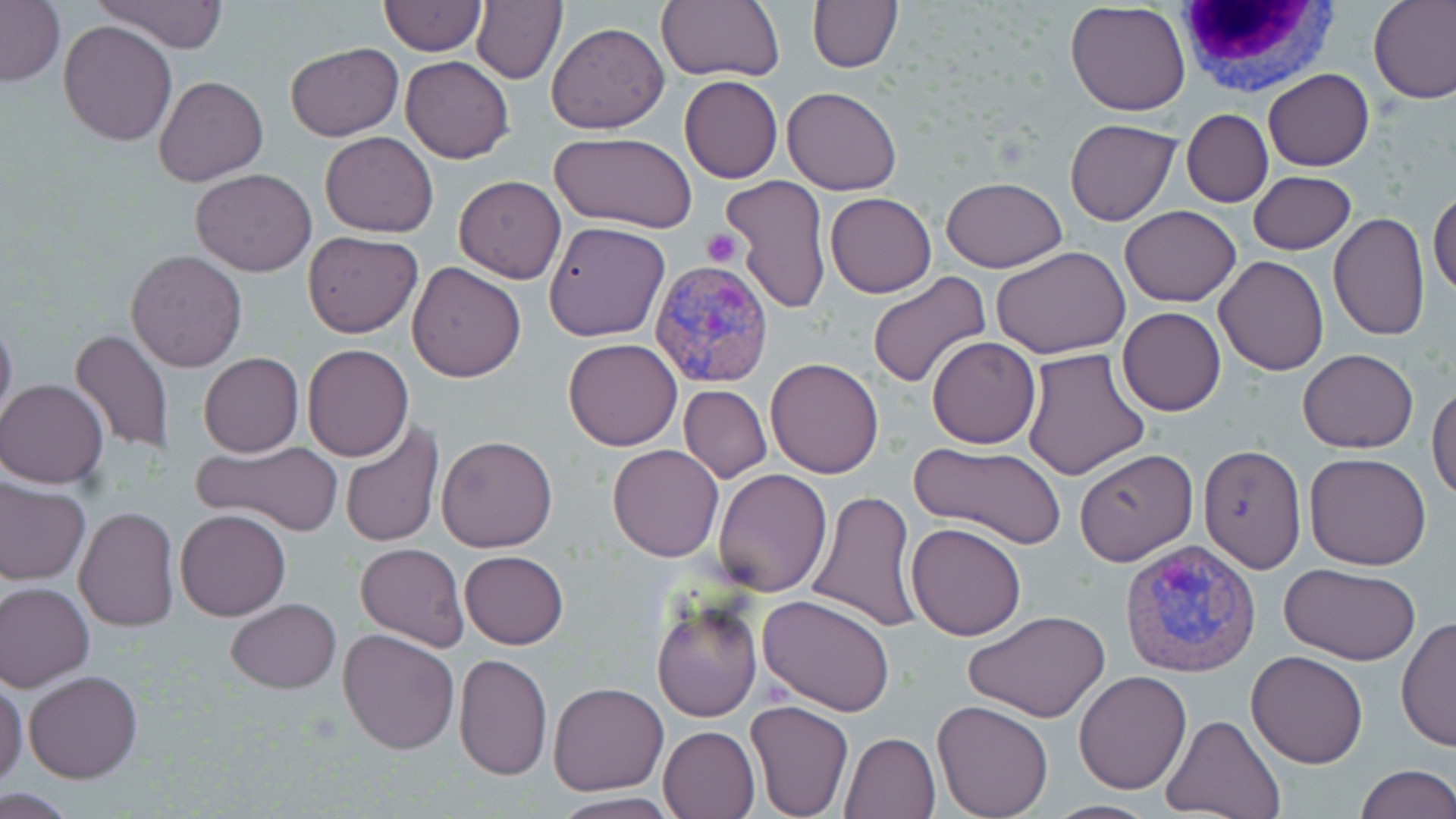
Approximate bounding boxes as (x1, y1, x2, y2) in pixels. White blood cell locations: (1173, 0, 1340, 103). Platelet locations: (702, 228, 744, 268). Uninfected red blood cell locations: (93, 0, 229, 53), (471, 0, 567, 85), (657, 0, 785, 81), (807, 0, 901, 73), (1369, 0, 1456, 105), (380, 1, 486, 55), (1, 2, 64, 87), (1065, 3, 1192, 116), (58, 21, 178, 147), (546, 21, 669, 133), (285, 42, 404, 141), (401, 57, 515, 164), (1263, 68, 1374, 171), (154, 75, 268, 187), (680, 76, 783, 183), (782, 86, 902, 196), (1183, 110, 1272, 207), (1065, 119, 1180, 226), (319, 131, 438, 237), (551, 133, 698, 235), (190, 169, 316, 276), (1250, 171, 1356, 255), (722, 174, 832, 313), (1266, 174, 1397, 286), (454, 175, 567, 284), (941, 176, 1066, 272), (1429, 187, 1456, 298), (824, 192, 935, 298), (1120, 205, 1240, 306), (1328, 213, 1430, 341), (542, 221, 669, 342), (303, 233, 421, 337), (991, 244, 1130, 359), (126, 249, 248, 372), (1213, 255, 1328, 376), (408, 262, 527, 382), (867, 273, 991, 390), (0, 305, 17, 436), (1117, 307, 1226, 416), (67, 328, 175, 457), (927, 337, 1040, 449), (564, 339, 682, 451), (303, 343, 413, 461), (1019, 348, 1152, 482), (1298, 350, 1418, 453), (199, 353, 304, 457), (764, 357, 884, 477), (1, 380, 109, 488), (678, 383, 771, 484), (1428, 383, 1456, 502), (338, 417, 444, 551), (436, 435, 558, 553), (192, 439, 342, 535), (909, 441, 1067, 549), (607, 444, 724, 562), (1198, 444, 1305, 574), (1074, 448, 1198, 565), (1304, 452, 1433, 570), (711, 468, 831, 596), (0, 476, 91, 585), (807, 489, 924, 634), (73, 506, 180, 633), (176, 509, 290, 620), (906, 522, 1028, 640), (356, 543, 467, 651), (459, 550, 568, 649), (1280, 563, 1423, 666), (0, 581, 95, 691), (757, 594, 898, 716), (652, 597, 761, 723), (226, 598, 340, 692), (964, 610, 1110, 722), (1397, 616, 1456, 754), (337, 627, 460, 755), (1245, 650, 1369, 768), (453, 653, 553, 781), (23, 669, 142, 783), (1074, 670, 1192, 794), (0, 679, 27, 790), (549, 681, 669, 796), (745, 699, 854, 818), (932, 700, 1054, 819), (1162, 715, 1287, 819), (659, 725, 761, 819), (840, 730, 941, 818), (1353, 764, 1456, 819), (548, 793, 682, 819), (1042, 801, 1163, 819). Plasmodium vivax-infected red blood cell locations: (648, 261, 775, 388), (1120, 536, 1261, 676). Slide-level diagnosis: Plasmodium vivax. Thin blood film. Single field of view. Optical microscopy. May-Grünwald-Giemsa-stained preparation. Image is 1456×819 pixels. 1000x magnification.